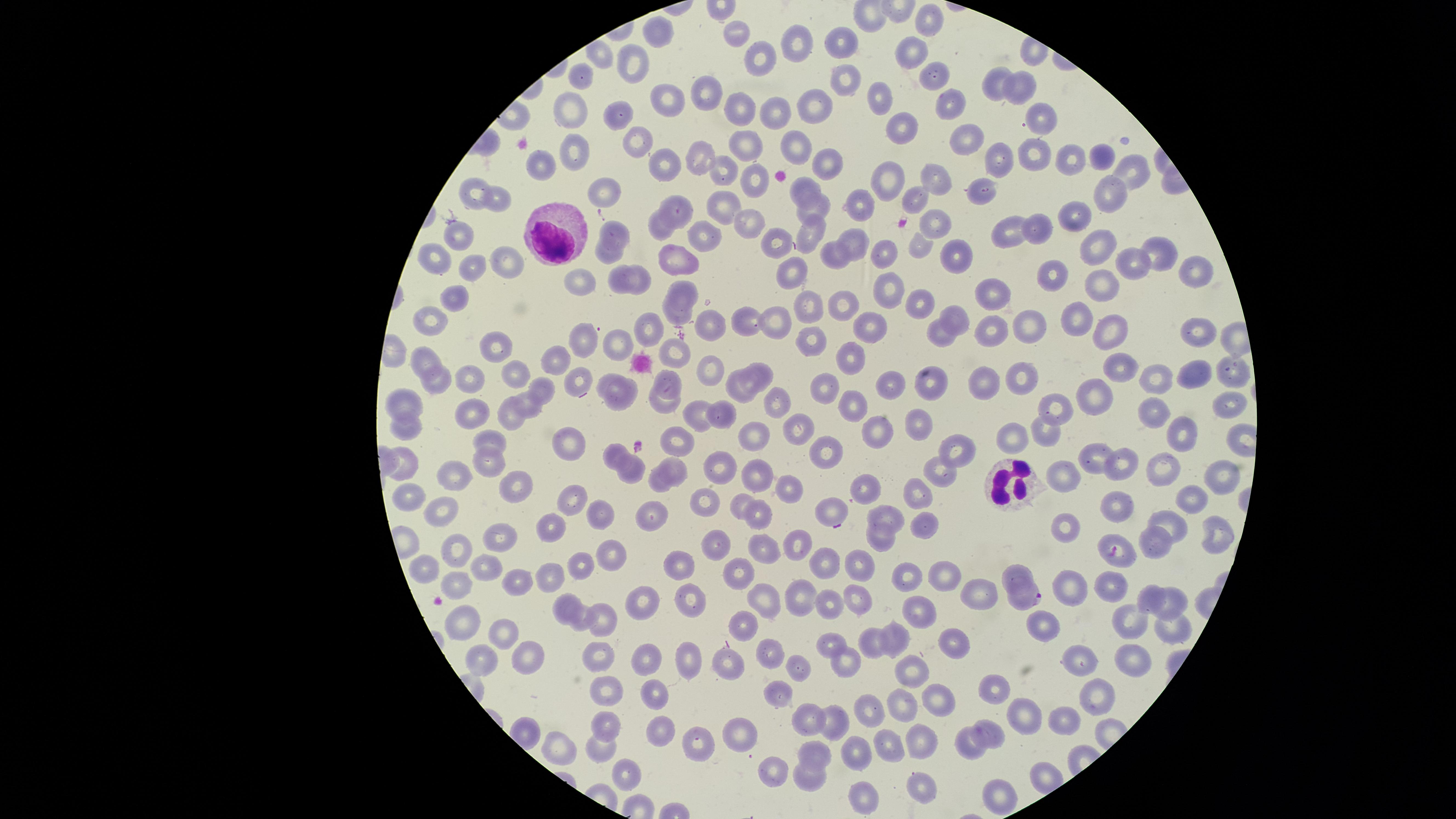

Approximate marker points as {x, y} in pixels.
Summary:
  - Parasitized red blood cells: {1116, 550}, {1026, 597}
  - White blood cells: {556, 235}, {1021, 479}
  - Uninfected red blood cells: {931, 22}, {664, 32}, {734, 36}, {848, 39}, {805, 41}, {913, 50}, {602, 56}, {631, 61}, {757, 61}, {583, 71}, {928, 75}, {844, 78}, {996, 86}, {1022, 88}, {708, 90}, {674, 96}, {871, 96}, {948, 102}, {740, 107}, {819, 107}, {575, 108}, {628, 113}, {782, 114}, {1043, 116}, {902, 124}, {959, 137}, {744, 142}, {644, 144}, {797, 146}, {575, 149}, {1031, 150}, {1102, 156}, {700, 157}, {1067, 157}, {1000, 159}, {828, 163}, {667, 164}, {546, 166}, {1134, 172}, {722, 174}, {891, 175}, {933, 177}, {753, 179}, {806, 186}, {478, 188}, {596, 190}, {501, 194}, {978, 196}, {1110, 196}, {916, 199}, {861, 208}, {721, 210}, {815, 211}, {679, 213}, {1074, 217}, {935, 219}, {662, 222}, {752, 223}, {1036, 225}, {616, 227}, {810, 233}, {705, 236}, {459, 237}, {1008, 237}, {776, 239}, {854, 242}, {920, 245}, {1091, 247}, {954, 248}, {1154, 251}, {612, 252}, {886, 253}, {430, 255}, {830, 257}, {678, 259}, {504, 264}, {1125, 266}, {793, 267}, {476, 268}, {1192, 271}, {1056, 273}, {637, 276}, {582, 284}, {619, 284}, {888, 284}, {1099, 286}, {992, 290}, {687, 293}, {455, 299}, {843, 302}, {912, 304}, {809, 310}, {677, 315}, {427, 318}, {955, 318}, {745, 319}, {775, 319}, {1074, 319}, {1021, 324}, {710, 325}, {990, 325}, {650, 326}, {1105, 327}, {868, 331}, {940, 336}, {1196, 336}, {811, 338}, {584, 343}, {496, 345}, {621, 346}, {422, 352}, {674, 354}, {854, 357}, {562, 364}, {1122, 368}, {1229, 369}, {763, 370}, {1186, 372}, {709, 373}, {517, 377}, {609, 377}, {472, 379}, {577, 380}, {885, 380}, {928, 380}, {1156, 380}, {669, 381}, {1021, 381}, {435, 382}, {978, 385}, {825, 386}, {742, 387}, {549, 390}, {621, 394}, {1090, 395}, {779, 400}, {408, 402}, {856, 403}, {667, 405}, {1055, 405}, {1230, 405}, {532, 410}, {470, 411}, {725, 413}, {1154, 413}, {699, 415}, {512, 416}, {877, 427}, {916, 427}, {406, 428}, {796, 430}, {1178, 435}, {755, 436}, {495, 438}, {570, 443}, {677, 446}, {614, 449}, {959, 452}, {829, 453}, {1092, 458}, {484, 462}, {409, 463}, {1123, 465}, {724, 468}, {675, 469}, {1168, 471}, {1219, 471}, {938, 473}, {759, 474}, {455, 476}, {630, 476}, {1067, 476}, {660, 479}, {513, 481}, {870, 486}, {783, 487}, {917, 490}, {404, 495}, {704, 498}, {573, 500}, {736, 501}, {1111, 502}, {1190, 502}, {439, 511}, {655, 513}, {758, 514}, {829, 514}, {599, 515}, {892, 518}, {925, 521}, {557, 522}, {1068, 525}, {1170, 526}, {875, 534}, {1215, 534}, {498, 540}, {722, 542}, {1155, 542}, {796, 543}, {455, 548}, {765, 548}, {602, 553}, {679, 564}, {822, 565}, {481, 566}, {581, 567}, {858, 567}, {427, 568}, {1018, 572}, {740, 573}, {909, 573}, {554, 575}, {947, 577}, {512, 582}, {456, 584}, {1113, 586}, {1075, 589}, {983, 593}, {1149, 593}, {692, 594}, {858, 595}, {797, 596}, {648, 601}, {829, 601}, {1176, 601}, {569, 602}, {760, 606}, {919, 610}, {1133, 618}, {602, 619}, {580, 622}, {746, 622}, {460, 625}, {1168, 625}, {508, 631}, {894, 632}, {830, 638}, {960, 641}, {867, 642}, {770, 647}, {650, 652}, {526, 654}, {483, 658}, {601, 659}, {1131, 659}, {845, 660}, {692, 662}, {1079, 663}, {728, 665}, {912, 667}, {802, 669}, {998, 685}, {781, 686}, {607, 688}, {1097, 691}, {658, 698}, {934, 698}, {903, 703}, {867, 708}, {1023, 716}, {1067, 720}, {806, 721}, {606, 724}, {831, 726}, {739, 730}, {998, 730}, {663, 731}, {702, 738}, {922, 742}, {973, 743}, {893, 745}, {598, 746}, {560, 747}, {861, 749}, {819, 751}, {775, 771}, {809, 772}, {624, 778}, {919, 787}, {995, 789}, {864, 794}
  - Visible region: circular
  - Presence: malaria parasites identified
  - Capture: smartphone photograph through the microscope eyepiece
  - Preparation: thin blood smear
  - Field of view: single
  - Species: Plasmodium falciparum
  - Stain: Giemsa
  - Image size: 1456×819 pixels